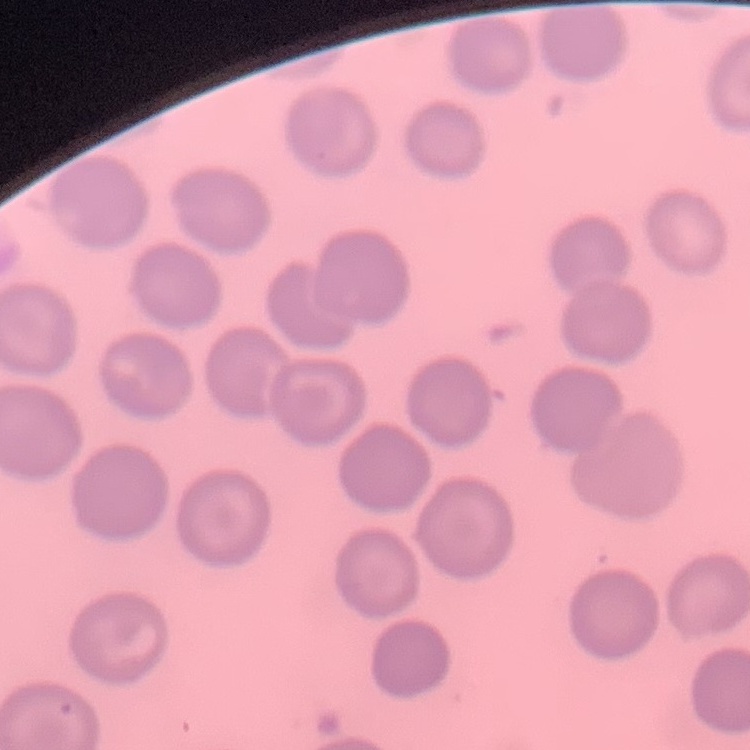

erythrocyte morphology = no rouleaux formation
image type = one tile cut from a larger photomicrograph
stain = Field's or Giemsa
preparation = thin blood film